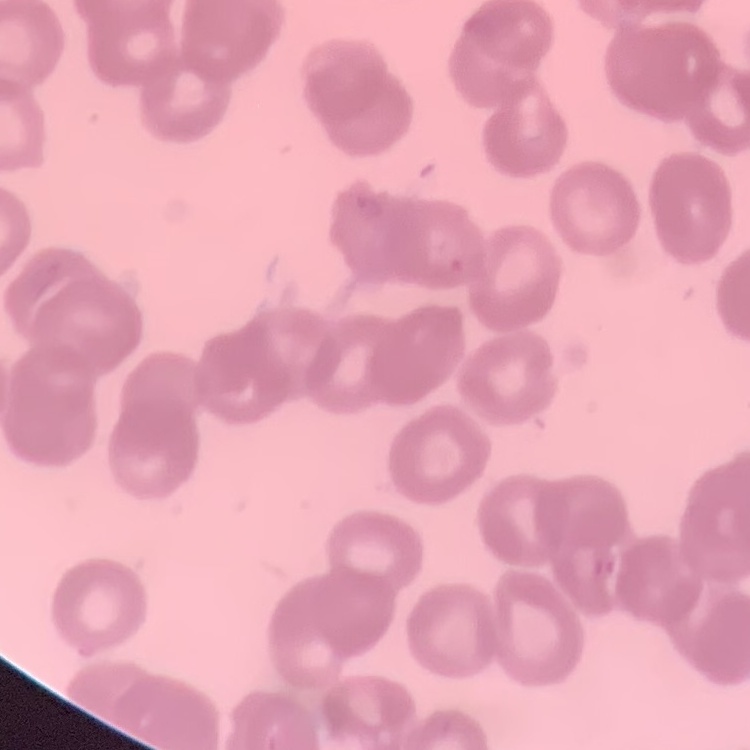
erythrocyte morphology = rouleaux formation
stain = Field's or Giemsa
preparation = thin peripheral smear
image type = one tile cut from a larger photomicrograph